Name the blood parasite species.
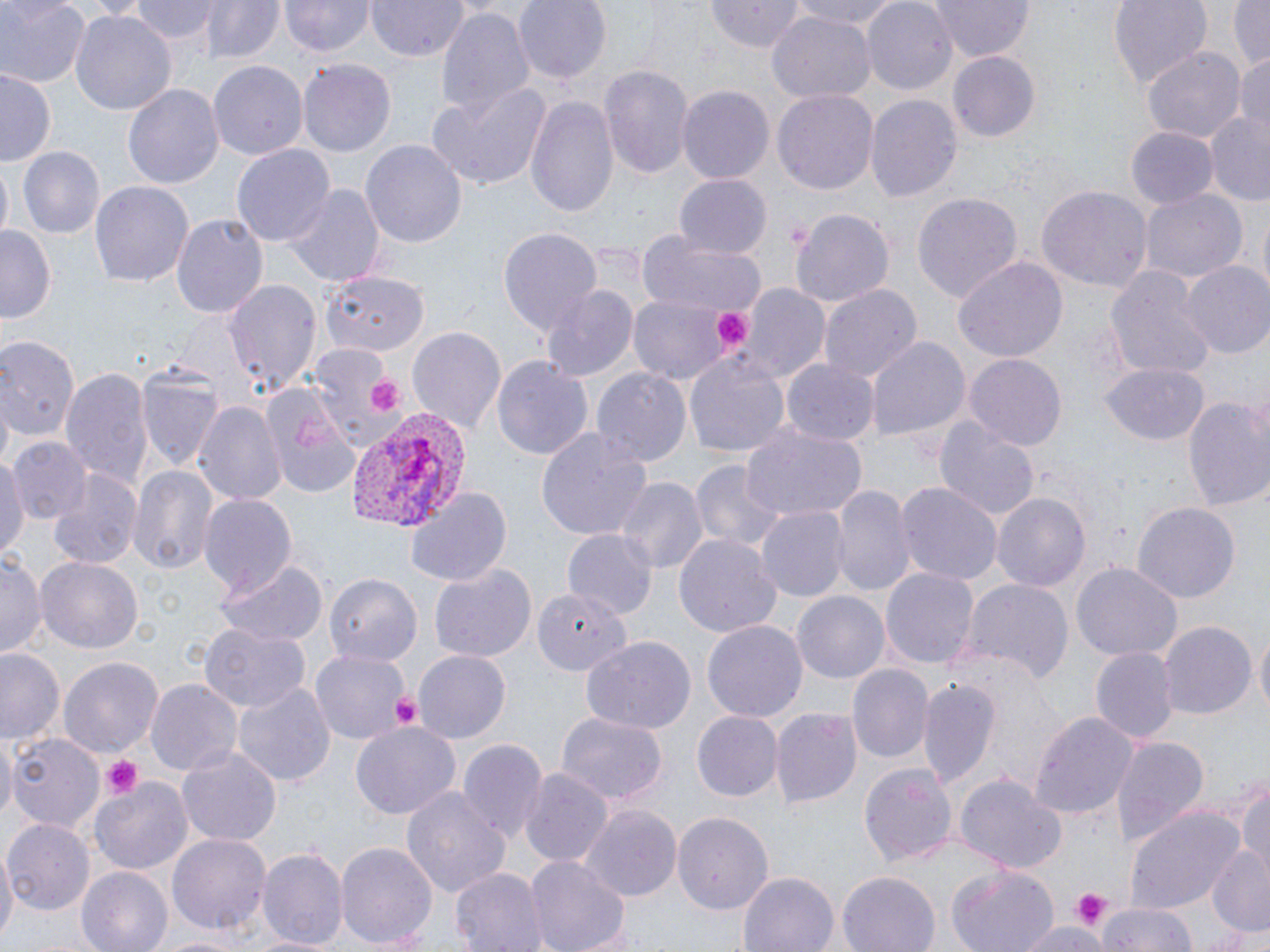
Plasmodium vivax.

field_of_view: single
stain: May-Grünwald-Giemsa
modality: optical microscopy
preparation: thin blood film
magnification: 1000x
image_size: 1270×952 pixels
platelet_locations: 'approximate bounding boxes as [x1, y1, x2, y2] in pixels: [715, 308, 753, 348], [368, 376, 406, 415], [388, 689, 424, 729], [99, 755, 141, 797], [1068, 889, 1114, 928]'
plasmodium_vivax_infected_red_blood_cell_locations: 'approximate bounding boxes as [x1, y1, x2, y2] in pixels: [343, 409, 467, 534]'
uninfected_red_blood_cell_locations: 'approximate bounding boxes as [x1, y1, x2, y2] in pixels: [0, 0, 86, 89], [130, 0, 218, 43], [201, 0, 282, 64], [281, 0, 374, 58], [368, 0, 467, 62], [513, 0, 611, 84], [706, 0, 805, 51], [785, 0, 909, 30], [862, 0, 958, 93], [928, 0, 1035, 62], [1108, 0, 1216, 87], [1229, 0, 1270, 71], [434, 5, 533, 124], [71, 9, 175, 118], [766, 13, 874, 103], [1143, 47, 1245, 141], [948, 51, 1039, 142], [1232, 52, 1270, 137], [207, 59, 307, 162], [298, 61, 395, 155], [599, 64, 694, 183], [1, 68, 58, 168], [424, 82, 552, 191], [125, 83, 223, 190], [677, 86, 774, 185], [773, 88, 879, 195], [525, 93, 620, 219], [865, 94, 960, 204], [1200, 115, 1269, 202], [1126, 126, 1217, 210], [360, 138, 468, 247], [231, 144, 335, 248], [18, 146, 104, 239], [0, 163, 13, 245], [673, 174, 773, 260], [90, 179, 192, 288], [286, 183, 384, 286], [1038, 186, 1151, 290], [1143, 189, 1246, 283], [913, 191, 1023, 304], [791, 208, 895, 307], [171, 214, 267, 322], [1, 225, 58, 324], [500, 228, 602, 341], [637, 229, 766, 320], [951, 256, 1068, 365], [1182, 262, 1270, 361], [1105, 266, 1216, 380], [321, 272, 426, 353], [224, 279, 322, 395], [740, 282, 829, 383], [540, 284, 639, 384], [818, 284, 921, 387], [629, 296, 735, 383], [406, 326, 505, 434], [866, 336, 972, 442], [0, 339, 103, 446], [305, 343, 401, 449], [684, 352, 791, 460], [964, 352, 1069, 449], [493, 356, 592, 462], [783, 359, 878, 446], [137, 362, 223, 474], [1102, 363, 1209, 447], [591, 364, 691, 467], [60, 367, 151, 490], [262, 388, 361, 499], [1183, 392, 1270, 517], [195, 402, 287, 506], [931, 414, 1042, 522], [738, 422, 868, 522], [537, 426, 653, 544], [11, 437, 91, 523], [24, 440, 127, 547], [0, 447, 25, 564], [689, 458, 790, 558], [127, 465, 218, 578], [45, 467, 145, 570], [615, 475, 705, 578], [833, 482, 912, 597], [897, 483, 1002, 587], [406, 486, 512, 585], [993, 491, 1091, 592], [199, 493, 296, 597], [1132, 504, 1237, 604], [756, 505, 849, 602], [563, 527, 657, 617], [674, 532, 781, 639], [0, 554, 45, 656], [37, 554, 142, 652], [214, 557, 328, 646], [428, 562, 536, 667], [1073, 563, 1180, 661], [881, 564, 978, 668], [324, 573, 421, 669], [964, 578, 1073, 688], [534, 586, 630, 674], [793, 592, 889, 683], [704, 620, 806, 722], [1160, 621, 1255, 719], [201, 624, 310, 711], [1254, 629, 1269, 721], [580, 635, 696, 734], [312, 646, 410, 743], [0, 647, 65, 748], [1090, 647, 1177, 743], [414, 651, 512, 743], [60, 656, 162, 758], [847, 664, 931, 762], [917, 678, 1000, 791], [147, 679, 241, 778], [233, 683, 337, 787], [771, 706, 862, 807], [1028, 708, 1137, 823], [693, 710, 783, 801], [556, 712, 663, 805], [351, 721, 460, 822], [0, 731, 18, 821], [9, 732, 103, 833], [1112, 734, 1208, 848], [457, 736, 547, 844], [176, 744, 282, 845], [859, 759, 958, 868], [519, 769, 613, 870], [954, 773, 1067, 872], [90, 777, 193, 874], [1235, 782, 1270, 873], [400, 787, 509, 903], [578, 805, 681, 905], [1125, 805, 1247, 913], [673, 811, 774, 915], [6, 819, 95, 915], [166, 833, 271, 938], [337, 841, 438, 952], [0, 844, 16, 950], [260, 847, 346, 950], [1206, 848, 1270, 936], [524, 855, 630, 952], [451, 865, 546, 952], [76, 866, 172, 952], [947, 866, 1061, 952], [738, 870, 838, 952], [837, 871, 940, 952], [1099, 898, 1200, 952], [1017, 920, 1109, 951]'